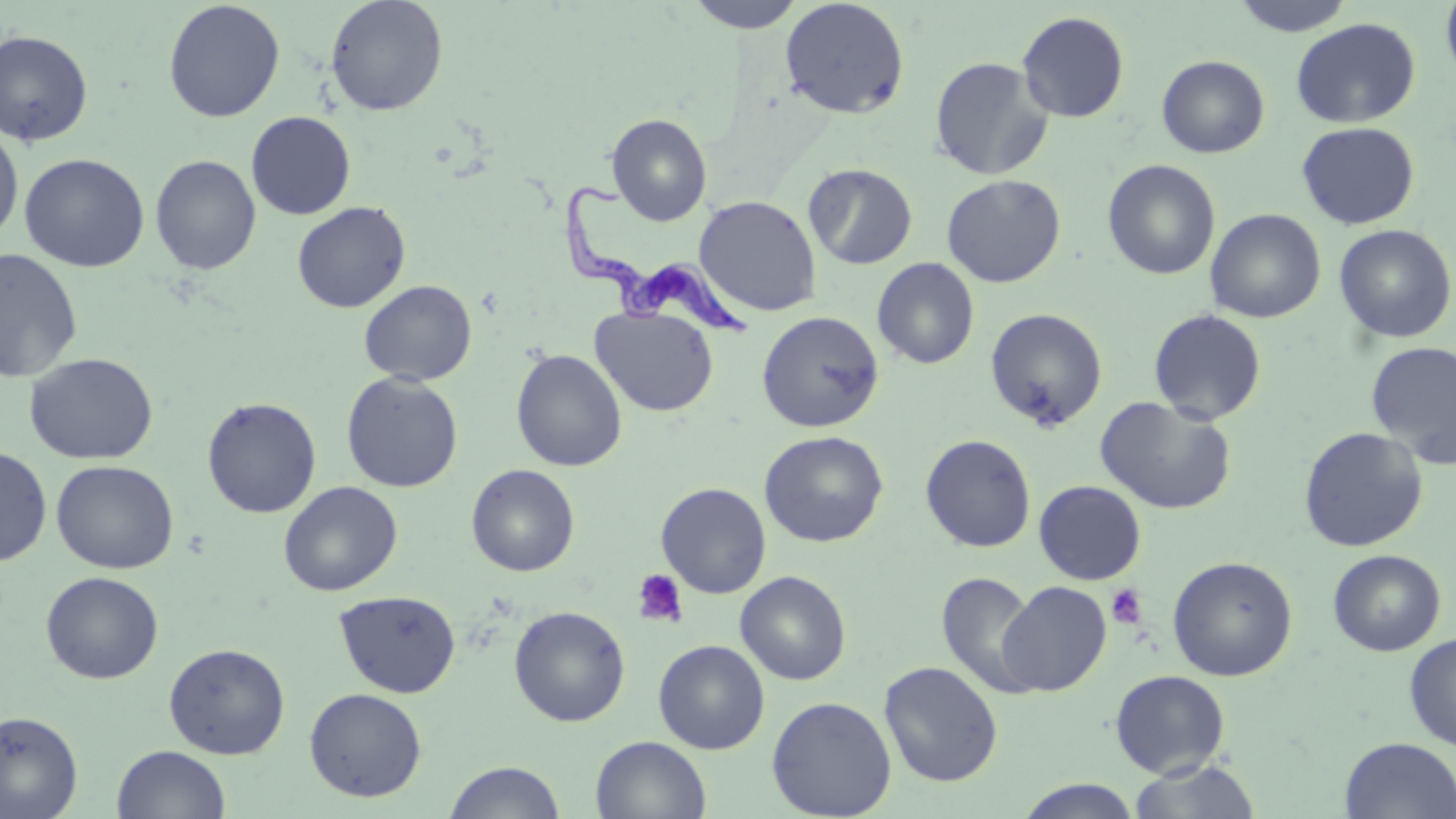
Approximate bounding boxes as named x1/y1/x2/y2 corners in pixels. Platelet locations: (x1=631, y1=568, x2=689, y2=628), (x1=1106, y1=584, x2=1147, y2=629). Uninfected red blood cell locations: (x1=324, y1=0, x2=449, y2=116), (x1=684, y1=0, x2=806, y2=33), (x1=1228, y1=0, x2=1357, y2=36), (x1=1439, y1=0, x2=1456, y2=90), (x1=162, y1=1, x2=285, y2=123), (x1=779, y1=1, x2=910, y2=119), (x1=1017, y1=11, x2=1129, y2=123), (x1=1290, y1=17, x2=1421, y2=128), (x1=0, y1=29, x2=94, y2=146), (x1=1156, y1=55, x2=1269, y2=158), (x1=929, y1=56, x2=1053, y2=181), (x1=246, y1=111, x2=356, y2=219), (x1=606, y1=113, x2=712, y2=226), (x1=1296, y1=122, x2=1420, y2=230), (x1=0, y1=125, x2=24, y2=244), (x1=19, y1=153, x2=150, y2=272), (x1=150, y1=154, x2=261, y2=274), (x1=1102, y1=159, x2=1220, y2=280), (x1=804, y1=163, x2=918, y2=269), (x1=941, y1=174, x2=1066, y2=288), (x1=694, y1=195, x2=822, y2=317), (x1=291, y1=201, x2=411, y2=313), (x1=1205, y1=208, x2=1326, y2=323), (x1=1334, y1=224, x2=1455, y2=344), (x1=1, y1=247, x2=84, y2=383), (x1=872, y1=257, x2=980, y2=369), (x1=359, y1=280, x2=477, y2=386), (x1=591, y1=306, x2=718, y2=417), (x1=985, y1=308, x2=1108, y2=430), (x1=1147, y1=308, x2=1267, y2=425), (x1=757, y1=311, x2=884, y2=433), (x1=1365, y1=341, x2=1456, y2=470), (x1=511, y1=349, x2=627, y2=472), (x1=24, y1=352, x2=158, y2=464), (x1=341, y1=372, x2=463, y2=492), (x1=1094, y1=396, x2=1237, y2=515), (x1=202, y1=397, x2=322, y2=518), (x1=1298, y1=426, x2=1428, y2=552), (x1=759, y1=430, x2=888, y2=547), (x1=920, y1=434, x2=1036, y2=552), (x1=0, y1=444, x2=52, y2=567), (x1=51, y1=460, x2=178, y2=574), (x1=467, y1=464, x2=580, y2=577), (x1=1034, y1=480, x2=1146, y2=584), (x1=278, y1=481, x2=403, y2=596), (x1=656, y1=482, x2=771, y2=598), (x1=1328, y1=549, x2=1446, y2=656), (x1=1167, y1=555, x2=1298, y2=681), (x1=41, y1=571, x2=163, y2=684), (x1=735, y1=571, x2=851, y2=685), (x1=936, y1=571, x2=1041, y2=698), (x1=996, y1=581, x2=1112, y2=696), (x1=333, y1=590, x2=461, y2=698), (x1=509, y1=605, x2=630, y2=727), (x1=1403, y1=632, x2=1456, y2=750), (x1=653, y1=639, x2=770, y2=754), (x1=164, y1=642, x2=290, y2=759), (x1=879, y1=660, x2=1004, y2=787), (x1=1110, y1=669, x2=1231, y2=778), (x1=304, y1=687, x2=427, y2=802), (x1=766, y1=696, x2=897, y2=818), (x1=0, y1=711, x2=83, y2=819), (x1=590, y1=735, x2=711, y2=819), (x1=1339, y1=736, x2=1456, y2=818), (x1=112, y1=745, x2=230, y2=819), (x1=1127, y1=759, x2=1262, y2=818), (x1=443, y1=760, x2=565, y2=818), (x1=1015, y1=778, x2=1143, y2=819). Trypanosoma brucei locations: (x1=561, y1=177, x2=752, y2=342). Slide-level diagnosis: Trypanosoma brucei. Image is 1456×819 pixels. 1000x magnification. Light microscopy. May-Grünwald-Giemsa stain. Thin blood film. Single field of view.